Assess this cell for malaria.
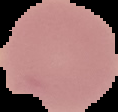
Uninfected.

Image is 118×112 pixels. Segmented cell region on a black background. From a thin blood smear.